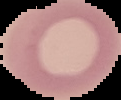

Summary:
  - Result: negative for Plasmodium parasites
  - Preparation: thin blood smear
  - Image type: segmented cell region with the area outside set to black
  - Image size: 121×100 pixels